Outline each blood parasite and name the species.
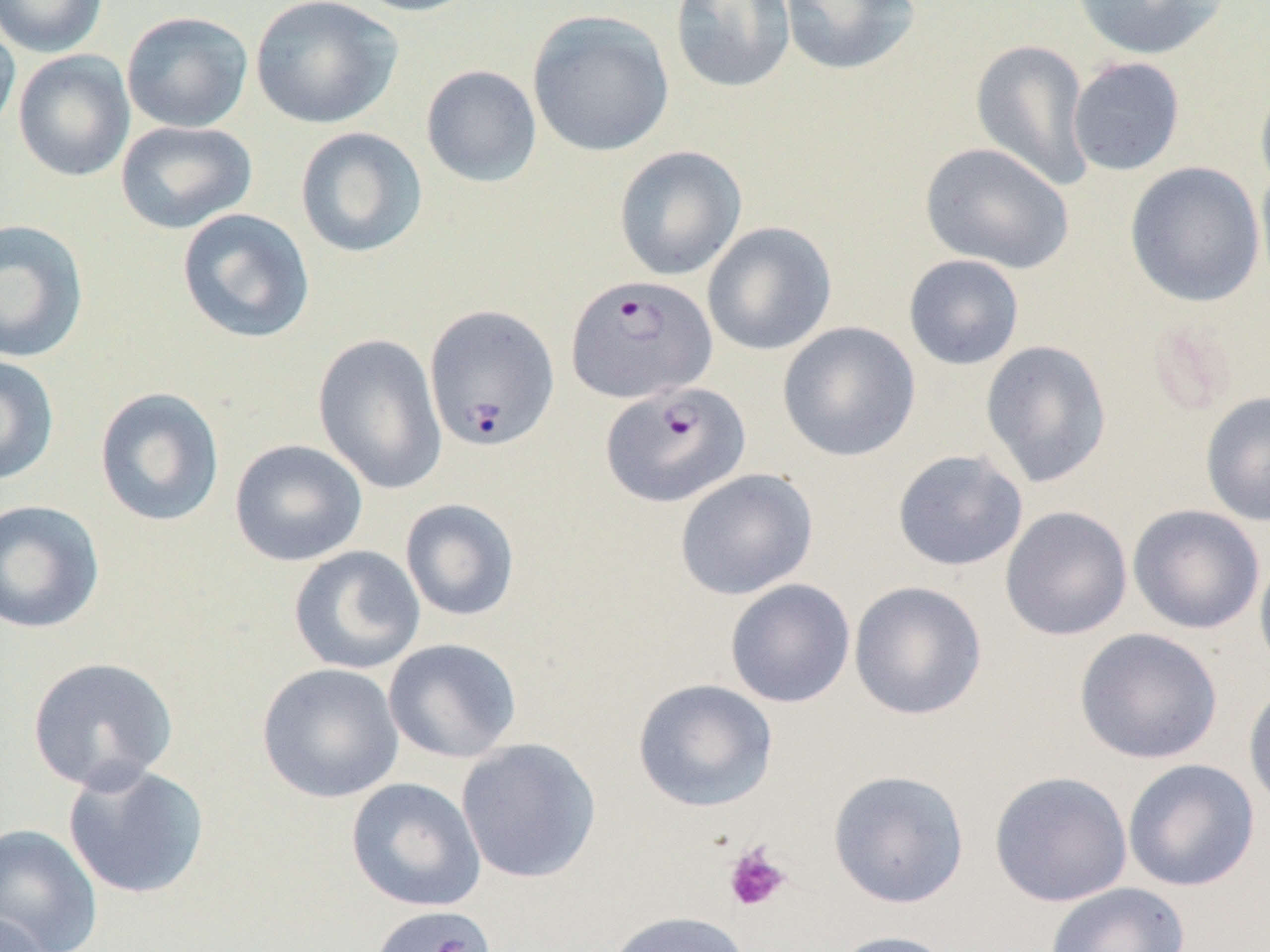

Approximate bounding boxes as (x1,y1)-(x2,y2) corner pairs in pixels.
Plasmodium falciparum-infected red blood cells: (565,274)-(717,404), (424,303)-(560,451), (601,381)-(751,508).
No Plasmodium ovale, Plasmodium malariae, Plasmodium vivax, Babesia divergens, or Trypanosoma brucei observed.

Summary:
  - Platelet locations: (722,843)-(791,913)
  - Uninfected red blood cell locations: (0,0)-(108,58), (250,0)-(402,130), (346,0)-(483,17), (669,0)-(796,94), (779,0)-(921,76), (1070,0)-(1230,60), (527,9)-(674,158), (121,11)-(253,134), (0,13)-(20,142), (970,39)-(1094,192), (13,50)-(136,182), (1067,57)-(1185,176), (420,64)-(542,188), (1255,74)-(1270,199), (115,120)-(258,234), (295,127)-(428,258), (919,142)-(1074,275), (613,145)-(747,281), (1124,161)-(1266,308), (1255,165)-(1270,297), (176,208)-(315,344), (0,218)-(90,363), (702,221)-(837,356), (903,254)-(1025,371), (776,321)-(921,462), (313,333)-(447,494), (980,339)-(1113,488), (0,354)-(60,486), (94,387)-(225,527), (1200,390)-(1270,527), (229,439)-(368,567), (892,449)-(1028,572), (674,468)-(819,600), (0,498)-(105,635), (400,498)-(520,622), (1128,504)-(1265,635), (999,505)-(1133,641), (288,545)-(425,674), (1254,548)-(1270,681), (724,579)-(856,708), (848,581)-(988,721), (1074,627)-(1223,764), (383,638)-(522,764), (26,656)-(178,793), (256,662)-(404,804), (632,678)-(778,812), (1243,681)-(1270,814), (456,738)-(602,884), (1122,758)-(1260,891), (62,762)-(210,900), (827,769)-(970,908), (988,771)-(1133,907), (346,777)-(486,912), (0,822)-(103,952), (1044,882)-(1190,952), (368,903)-(498,951), (1,908)-(54,952), (603,910)-(752,952), (827,930)-(961,952)
  - Slide-level diagnosis: Plasmodium falciparum
  - Magnification: 1000x
  - Field of view: one of a larger specimen
  - Modality: light microscopy
  - Preparation: thin blood film
  - Image size: 1270×952 pixels